Outline each P. falciparum parasite and classify it by life-cycle stage.
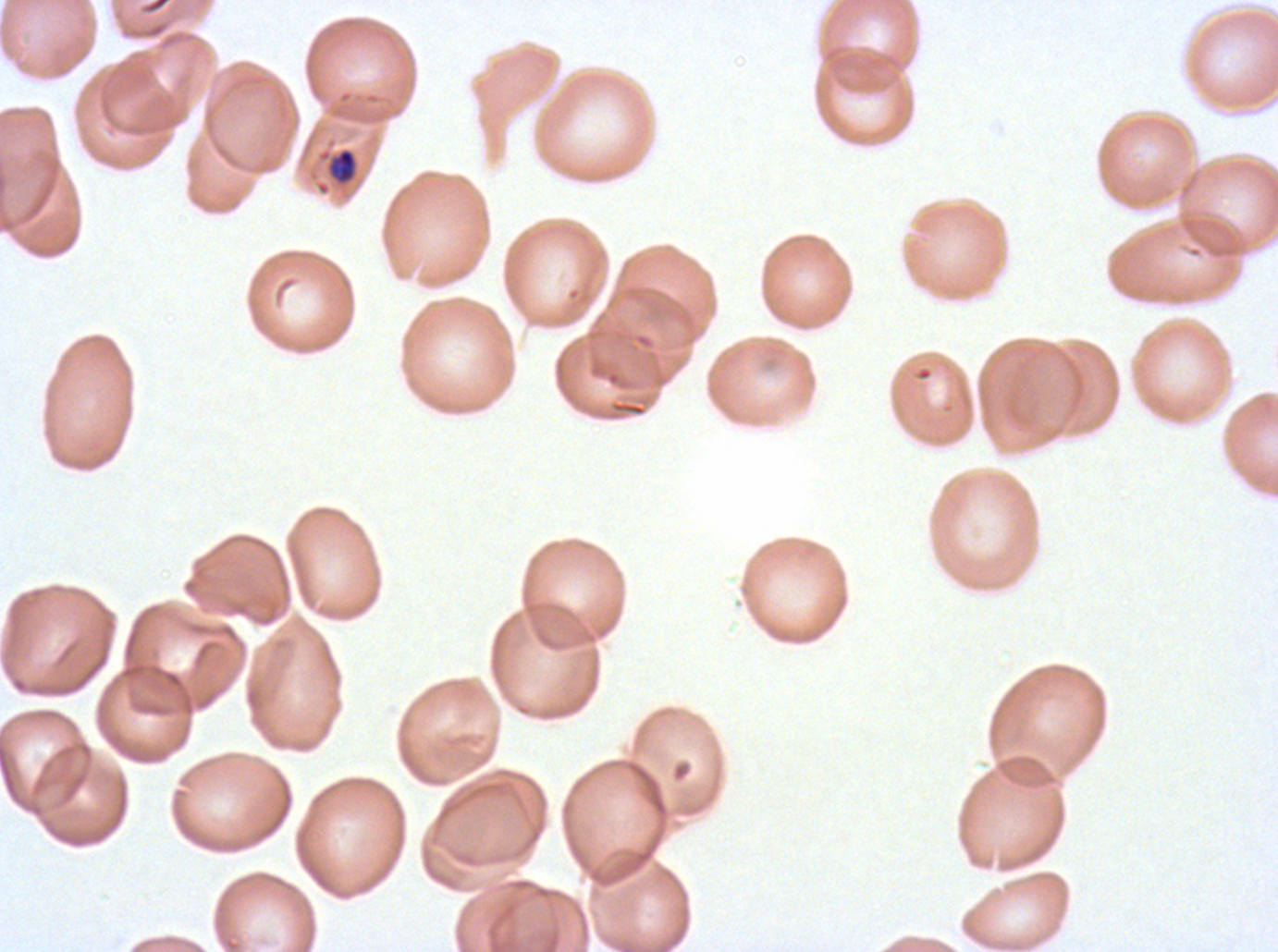
Approximate bounding boxes as (x1, y1, x2, y2) in pixels.
Late-ring/early-trophozoite forms: (316, 145, 361, 189).
No rings, mid trophozoites, late trophozoites, early schizonts, late schizonts, segmenters, or gametocytes observed.

One sub-image of a larger composite. Image is 1278×952 pixels. Giemsa-stained preparation. P. falciparum cultured ex vivo for 24 to 48 hours, from a patient in The Gambia. Thin blood film.